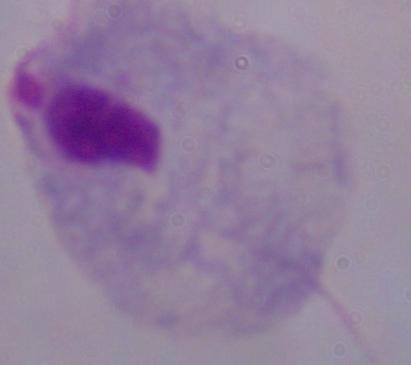
Summary:
  - Identification: trichomonad
  - Magnification: 1000x
  - Modality: micrograph